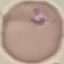 Result: malaria parasites identified. Thin blood film. Giemsa stain. Photographed with a smartphone camera at the microscope eyepiece. Automatically extracted cell patch, resized to 64 × 64 pixels.